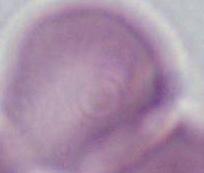

modality = micrograph
identification = red blood cell
magnification = 1000x